State which cell type is depicted.
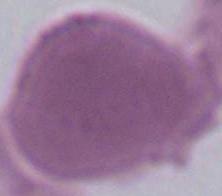
This is an erythrocyte.

magnification = 1000x
modality = photomicrograph